Locate every Plasmodium parasite.
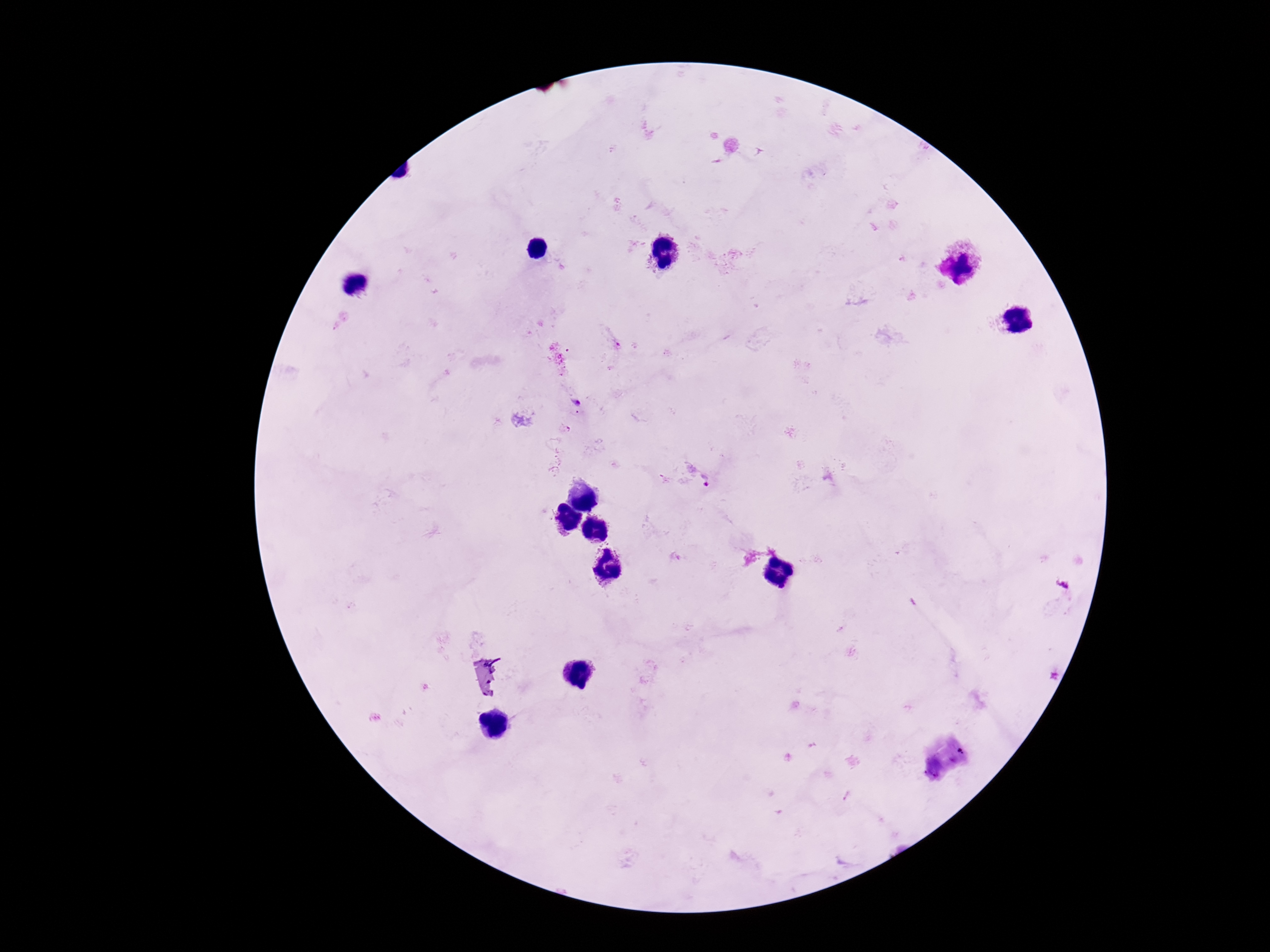

Approximate centers as (x, y) in pixels.
Plasmodium parasites: (576, 403), (704, 481).

image size = 1270×952 pixels
capture = smartphone camera through the microscope eyepiece
preparation = thick blood film
patient malaria status = infected
field of view = one from this slide
magnification = 100x
stain = Giemsa